State the blood parasite species.
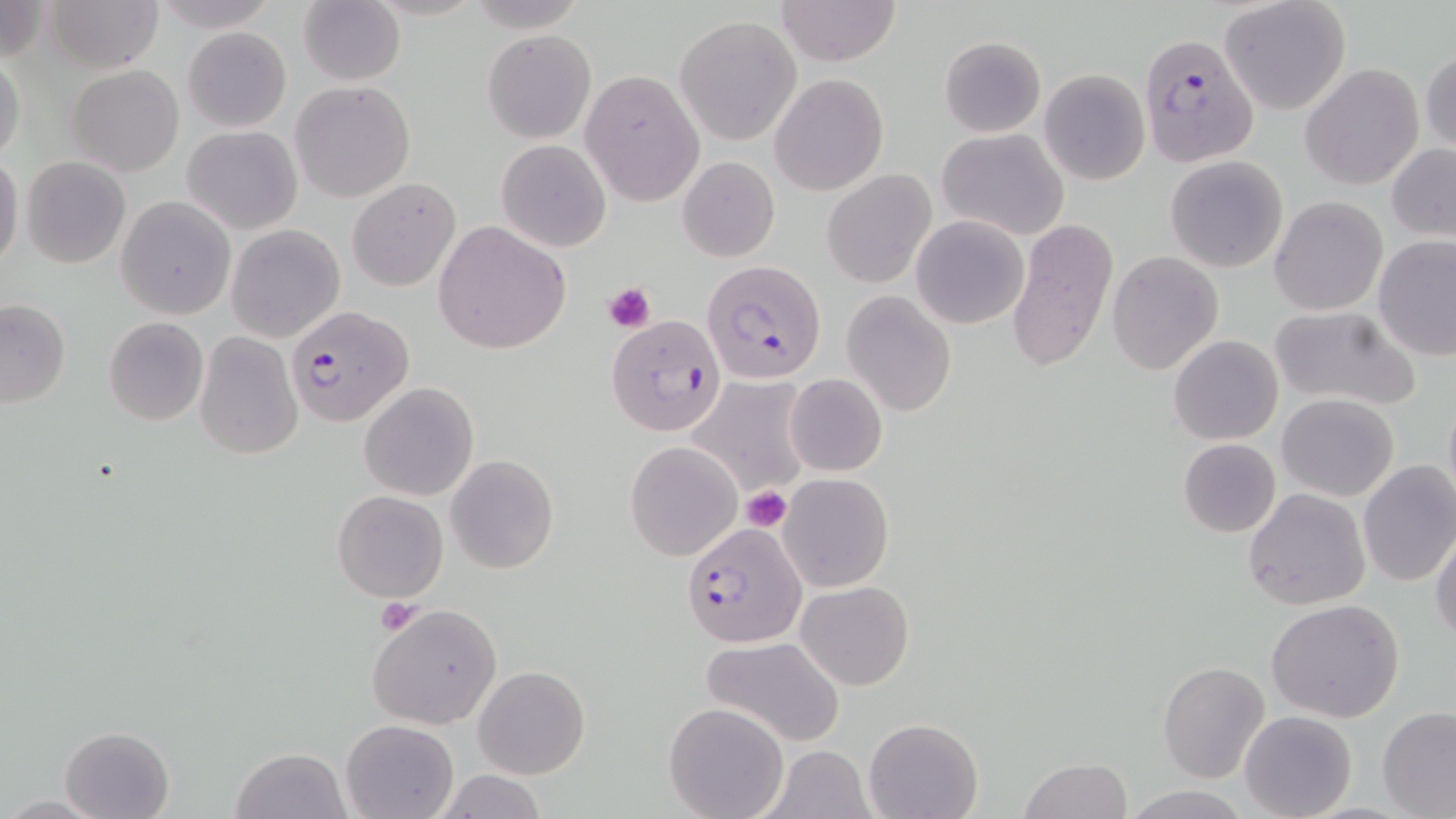
Plasmodium falciparum.

Approximate bounding boxes as (x1, y1, x2, y2) in pixels. Platelet locations: (604, 281, 656, 334), (741, 486, 791, 529), (375, 598, 425, 634). Plasmodium falciparum-infected red blood cell locations: (1137, 32, 1261, 168), (705, 267, 823, 378), (288, 304, 412, 428), (606, 314, 726, 438), (680, 523, 806, 649). Uninfected red blood cell locations: (43, 0, 162, 72), (156, 0, 274, 30), (776, 0, 901, 66), (1219, 1, 1352, 116), (299, 3, 404, 85), (675, 16, 801, 144), (182, 28, 291, 131), (483, 31, 595, 142), (939, 36, 1046, 136), (1420, 42, 1455, 160), (0, 53, 25, 167), (1300, 63, 1423, 190), (67, 65, 183, 175), (1039, 67, 1151, 186), (581, 69, 703, 205), (770, 73, 888, 194), (290, 80, 417, 201), (182, 125, 301, 234), (938, 128, 1068, 240), (495, 139, 611, 252), (1387, 144, 1456, 244), (0, 156, 25, 267), (21, 156, 131, 268), (677, 156, 780, 262), (1164, 156, 1288, 271), (822, 168, 937, 288), (347, 178, 460, 291), (1269, 195, 1388, 316), (116, 196, 236, 319), (912, 216, 1029, 329), (1006, 218, 1118, 372), (434, 221, 570, 354), (227, 224, 345, 344), (1373, 236, 1455, 360), (1107, 251, 1223, 374), (843, 291, 956, 415), (0, 300, 70, 408), (1268, 304, 1423, 414), (103, 317, 209, 426), (195, 333, 303, 459), (1169, 335, 1283, 445), (689, 359, 814, 495), (784, 373, 888, 477), (359, 382, 478, 501), (1442, 388, 1456, 508), (1277, 393, 1399, 501), (1177, 438, 1280, 537), (624, 441, 740, 561), (446, 456, 559, 574), (1357, 460, 1456, 587), (778, 473, 894, 592), (1242, 488, 1370, 610), (332, 490, 448, 601), (1431, 530, 1456, 647), (795, 579, 913, 691), (1266, 598, 1405, 723), (367, 605, 502, 729), (703, 637, 845, 748), (1158, 661, 1269, 784), (474, 665, 590, 780), (663, 700, 788, 819), (1376, 707, 1455, 817), (1240, 710, 1357, 819), (864, 717, 983, 819), (340, 718, 458, 819), (60, 725, 176, 819), (766, 745, 873, 819), (229, 747, 350, 819), (1020, 758, 1131, 819), (433, 770, 550, 818). Image is 1456×819 pixels. Light microscopy. Single field of view. Thin blood film. May-Grünwald-Giemsa stain. 1000x magnification.